Give the position of every leukocyte.
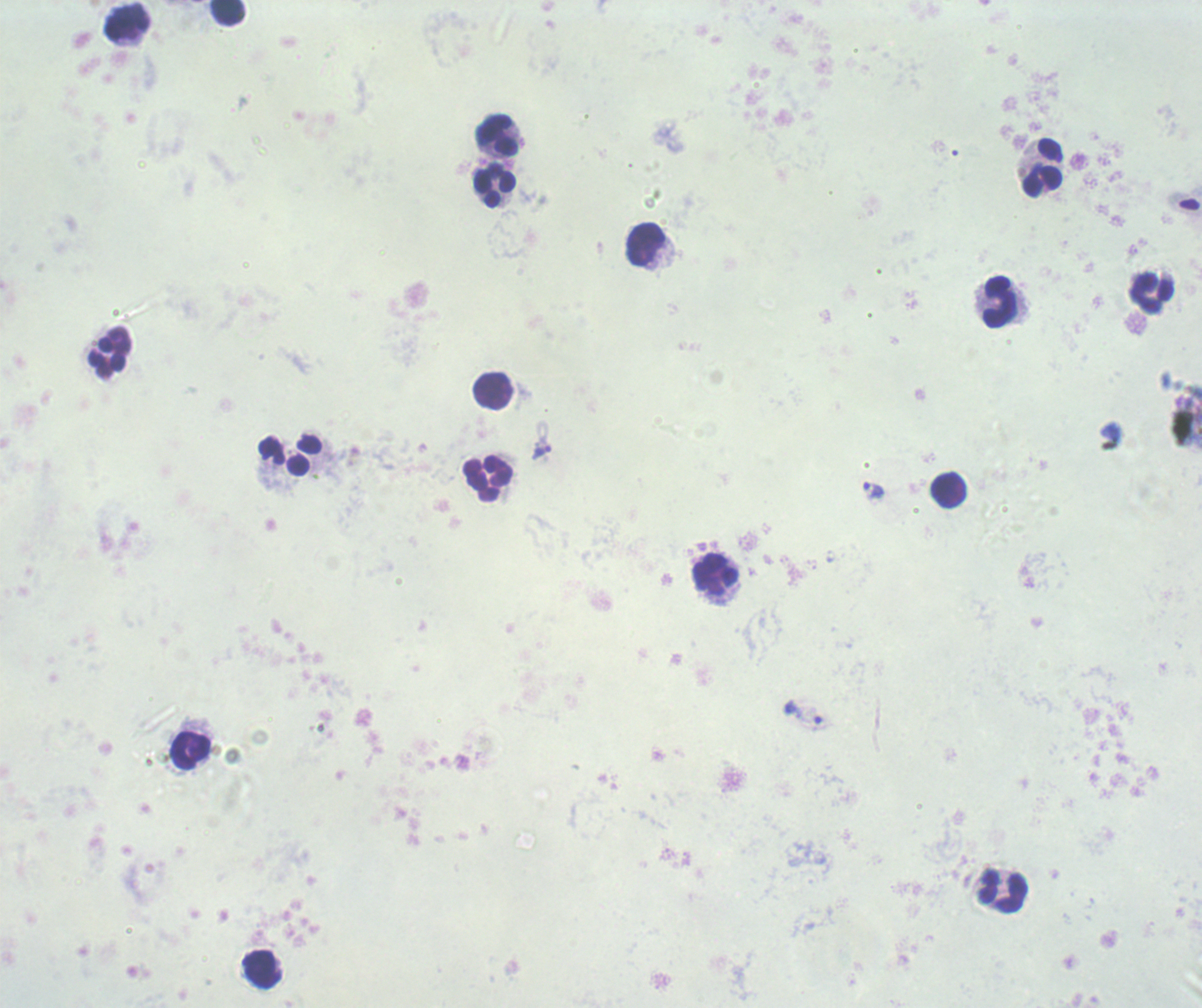

Approximate centers as (x, y) in pixels.
Leukocytes: (227, 12), (126, 22), (497, 135), (1043, 168), (494, 186), (646, 245), (1152, 293), (999, 302), (110, 353), (493, 390), (290, 453), (488, 480), (949, 490), (716, 576), (191, 750), (1003, 892), (262, 969).

Approximate centers as (x, y) in pixels.
Summary:
  - Trophozoite locations: (540, 452), (872, 491), (803, 713)
  - Result: positive for Plasmodium parasites
  - Background quality: unsatisfactory
  - Magnification: 100x
  - Field of view: one from this slide
  - Image size: 1202×1008 pixels
  - Stain: Romanowsky
  - Preparation: thick blood film
  - Context: previously used in an actual diagnosis